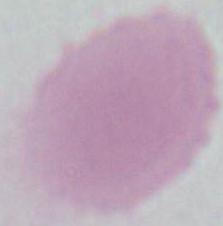

modality = micrograph
magnification = 1000x
identification = erythrocyte